Classify this cell by malaria status.
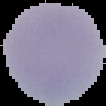

Uninfected.

preparation: thin blood smear
image_type: segmented cell region with the area outside set to black
image_size: 106×106 pixels